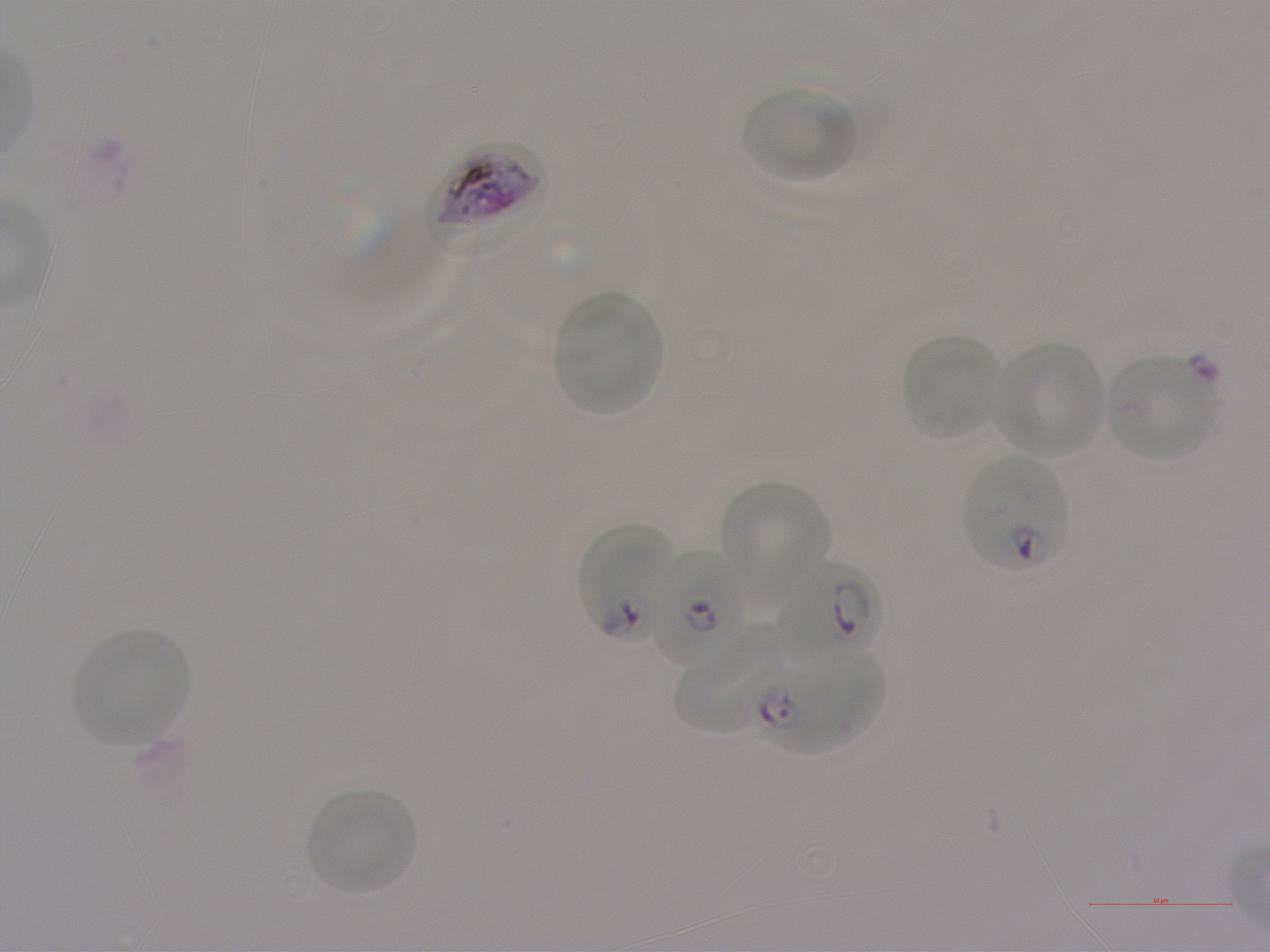
Approximate bounding boxes as {x1, y1, x2, y2} in pixels. Not every red blood cell is marked. A life-cycle stage — or a range of stages, where the recorded stages span more than one — follows each staged infected red blood cell.
Summary:
  - Locations of uninfected red blood cells: {740, 86, 859, 183}, {554, 292, 661, 415}, {900, 333, 1000, 440}, {994, 341, 1106, 458}, {1107, 355, 1217, 461}, {720, 479, 828, 608}, {674, 621, 787, 735}, {74, 629, 192, 746}, {307, 789, 419, 896}
  - Locations of infected red blood cells: {434, 143, 550, 251}; {961, 456, 1071, 574} ring; {577, 525, 673, 644} ring; {650, 549, 748, 670} ring; {775, 559, 883, 664} early ring to early trophozoite; {759, 649, 885, 753} ring
  - Objective: 100x, oil immersion, numerical aperture 1.25
  - Preparation: thin blood smear
  - Field of view: one from this slide
  - Donor blood group: A+
  - Stain: Giemsa
  - Image size: 1270×952 pixels
  - Culture: static in-vitro P. falciparum strain NF54